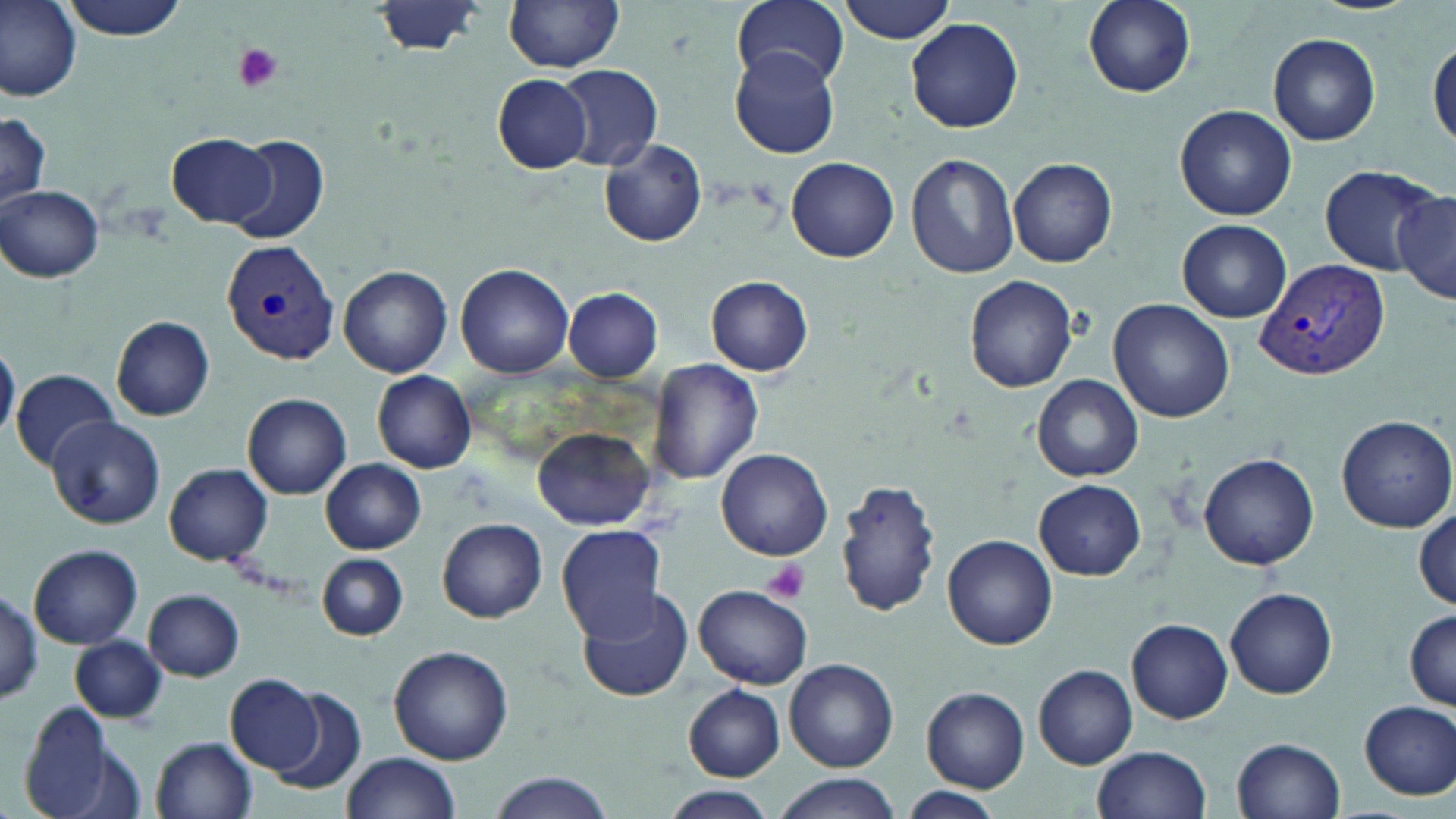
Summary:
  - Coordinate format: approximate bounding boxes as named x1/y1/x2/y2 corners in pixels
  - Platelet locations: (x1=231, y1=42, x2=285, y2=94), (x1=761, y1=560, x2=811, y2=603)
  - Plasmodium vivax-infected red blood cell locations: (x1=222, y1=241, x2=338, y2=366), (x1=1257, y1=259, x2=1391, y2=385)
  - Uninfected red blood cell locations: (x1=0, y1=0, x2=81, y2=102), (x1=59, y1=0, x2=189, y2=41), (x1=504, y1=0, x2=625, y2=73), (x1=734, y1=0, x2=849, y2=90), (x1=836, y1=0, x2=957, y2=43), (x1=1082, y1=0, x2=1194, y2=97), (x1=370, y1=1, x2=486, y2=58), (x1=906, y1=17, x2=1024, y2=133), (x1=1268, y1=32, x2=1381, y2=147), (x1=1429, y1=39, x2=1456, y2=149), (x1=729, y1=48, x2=842, y2=159), (x1=554, y1=65, x2=662, y2=173), (x1=491, y1=73, x2=591, y2=172), (x1=1174, y1=104, x2=1296, y2=220), (x1=0, y1=113, x2=50, y2=210), (x1=166, y1=134, x2=275, y2=228), (x1=228, y1=136, x2=330, y2=245), (x1=600, y1=140, x2=707, y2=246), (x1=906, y1=153, x2=1019, y2=280), (x1=787, y1=157, x2=899, y2=261), (x1=1007, y1=157, x2=1117, y2=269), (x1=1318, y1=166, x2=1440, y2=275), (x1=1, y1=185, x2=103, y2=282), (x1=1391, y1=190, x2=1455, y2=305), (x1=1176, y1=219, x2=1292, y2=322), (x1=456, y1=264, x2=574, y2=378), (x1=340, y1=266, x2=452, y2=378), (x1=706, y1=276, x2=811, y2=377), (x1=964, y1=276, x2=1079, y2=392), (x1=563, y1=288, x2=664, y2=383), (x1=1109, y1=298, x2=1237, y2=424), (x1=111, y1=317, x2=215, y2=421), (x1=0, y1=343, x2=20, y2=444), (x1=650, y1=358, x2=762, y2=486), (x1=11, y1=370, x2=115, y2=467), (x1=372, y1=370, x2=476, y2=473), (x1=1033, y1=375, x2=1143, y2=482), (x1=243, y1=393, x2=351, y2=498), (x1=1334, y1=413, x2=1456, y2=532), (x1=46, y1=416, x2=165, y2=529), (x1=532, y1=427, x2=656, y2=531), (x1=716, y1=448, x2=833, y2=561), (x1=1199, y1=453, x2=1321, y2=571), (x1=320, y1=458, x2=426, y2=554), (x1=164, y1=463, x2=272, y2=566), (x1=836, y1=477, x2=944, y2=617), (x1=1033, y1=478, x2=1146, y2=581), (x1=1413, y1=510, x2=1456, y2=610), (x1=439, y1=518, x2=546, y2=622), (x1=556, y1=524, x2=666, y2=641), (x1=944, y1=535, x2=1057, y2=650), (x1=29, y1=544, x2=143, y2=649), (x1=315, y1=555, x2=409, y2=640), (x1=696, y1=584, x2=812, y2=689), (x1=575, y1=585, x2=694, y2=703), (x1=1225, y1=586, x2=1337, y2=699), (x1=143, y1=588, x2=244, y2=680), (x1=0, y1=590, x2=44, y2=700), (x1=1404, y1=610, x2=1456, y2=709), (x1=1125, y1=617, x2=1233, y2=723), (x1=69, y1=635, x2=167, y2=723), (x1=387, y1=645, x2=513, y2=764), (x1=784, y1=658, x2=898, y2=770), (x1=1034, y1=665, x2=1136, y2=767), (x1=226, y1=676, x2=325, y2=774), (x1=683, y1=685, x2=785, y2=781), (x1=272, y1=687, x2=366, y2=795), (x1=921, y1=687, x2=1029, y2=792), (x1=1358, y1=699, x2=1456, y2=799), (x1=19, y1=702, x2=115, y2=818), (x1=152, y1=736, x2=258, y2=818), (x1=1232, y1=737, x2=1346, y2=819), (x1=1092, y1=746, x2=1212, y2=819), (x1=341, y1=752, x2=461, y2=819), (x1=491, y1=773, x2=616, y2=819), (x1=771, y1=775, x2=899, y2=819), (x1=665, y1=787, x2=773, y2=819), (x1=900, y1=788, x2=1006, y2=819)
  - Slide-level diagnosis: Plasmodium vivax
  - Field of view: one of a larger specimen
  - Preparation: thin blood film
  - Modality: light microscopy
  - Magnification: 1000x
  - Image size: 1456×819 pixels
  - Stain: May-Grünwald-Giemsa